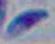
identification = Toxoplasma gondii
modality = micrograph
magnification = 1000x